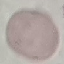

malaria_status: uninfected
image_type: automatically extracted cell patch, resized to 64 × 64 pixels
preparation: thin blood smear
stain: Giemsa
capture: smartphone through the microscope eyepiece